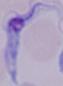

modality: micrograph
magnification: 1000x
identification: trypanosome